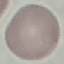
malaria_status: uninfected
preparation: thin smear
capture: smartphone camera at the microscope eyepiece
stain: Giemsa
image_type: cell patch, automatically extracted from a larger field of view and resized to 64 × 64 pixels